Assess for malaria.
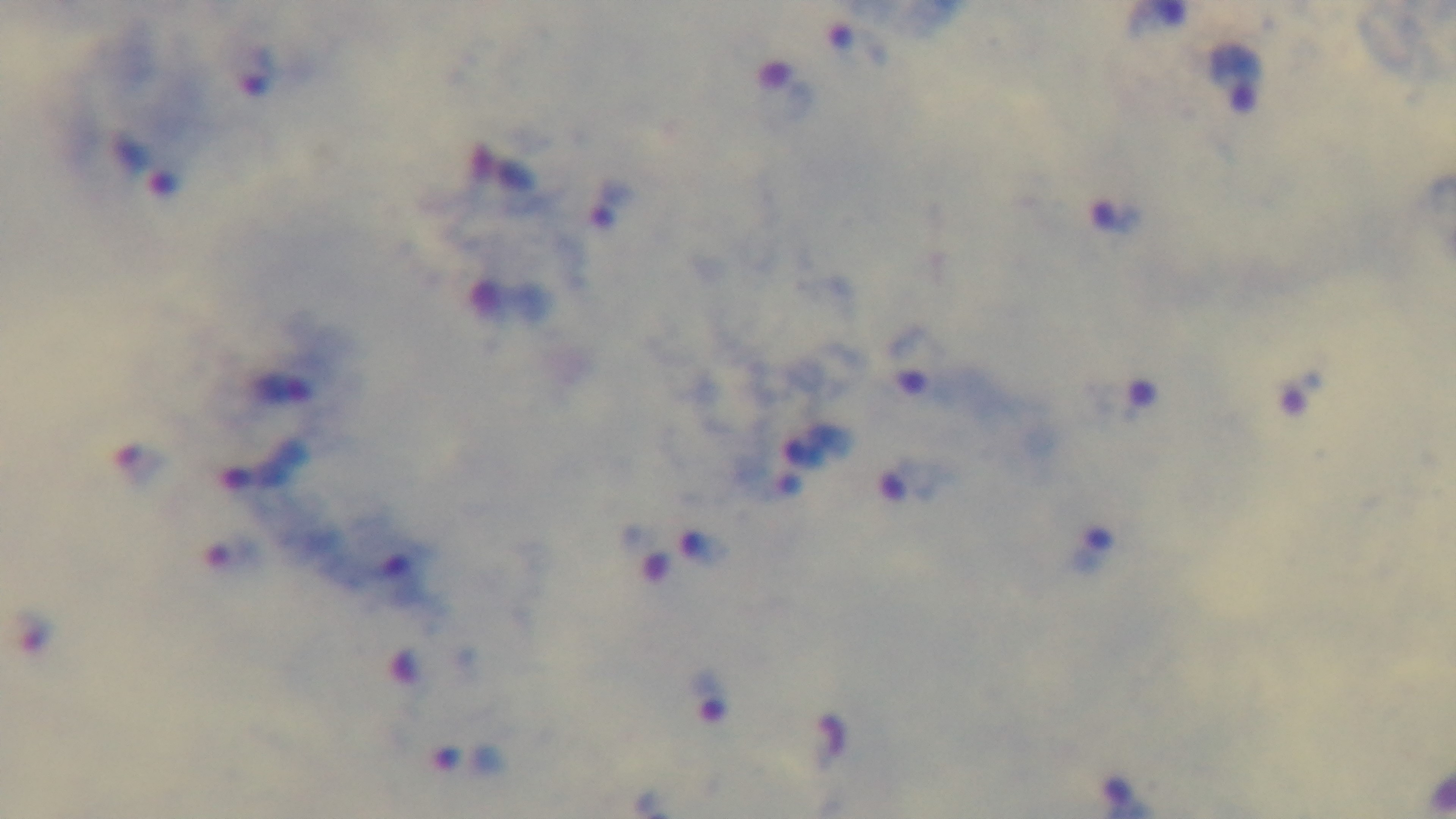
Infected.

preparation = thick
field of view = one from the slide
modality = light microscopy
capture = mounted 4K digital camera
stain = Giemsa
objective = 100x oil immersion